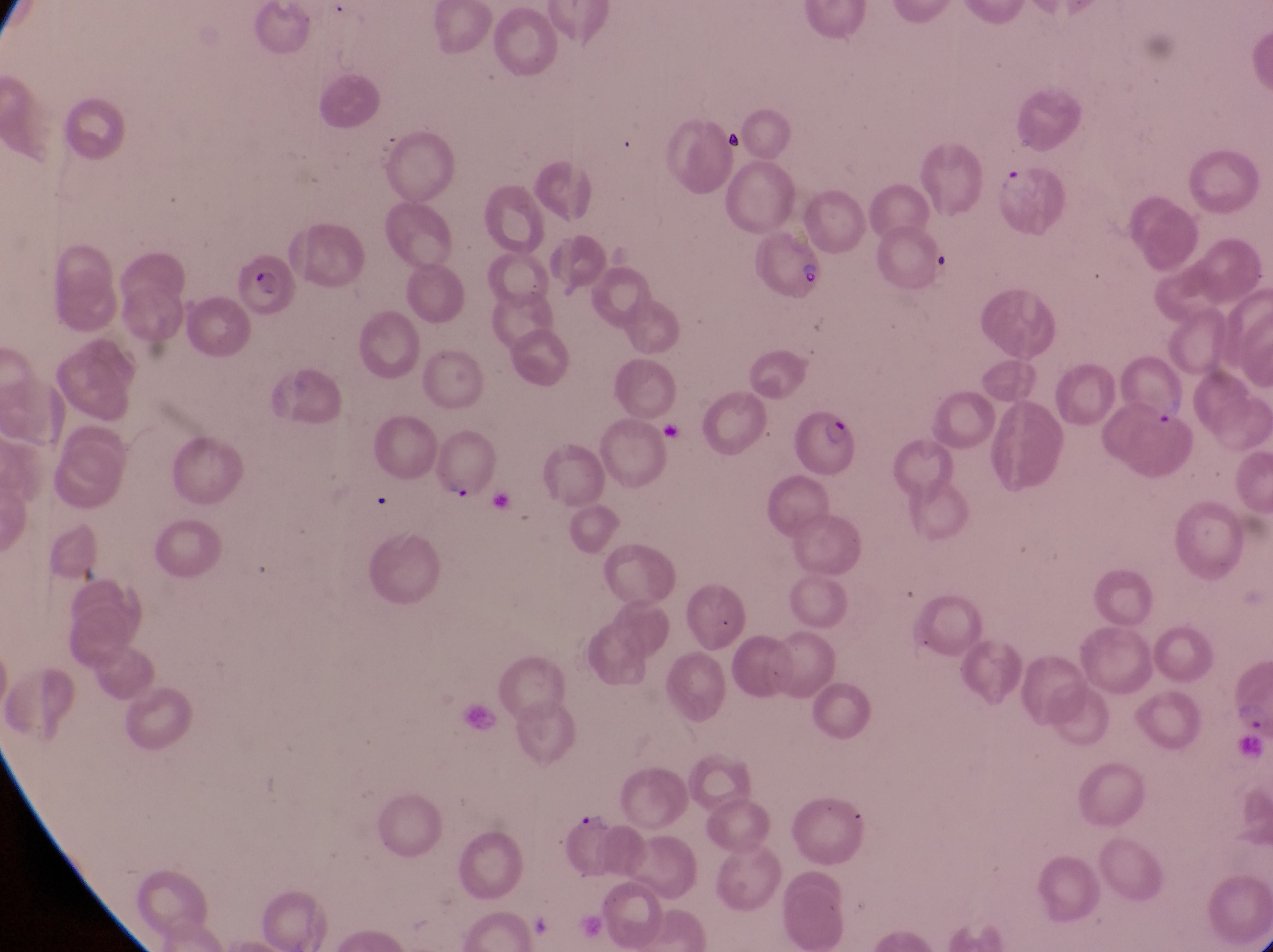

Approximate bounding boxes as (left, top, right, bottom) in pixels. Artifact (platelet-like body, stain precipitate, or debris) locations: (717, 123, 750, 155). Parasitised red blood cell locations: (996, 157, 1070, 240), (752, 223, 829, 298), (232, 262, 297, 324), (1120, 344, 1192, 429), (791, 404, 860, 479). Trophozoite locations: (444, 474, 477, 507), (1231, 696, 1270, 739), (576, 807, 613, 834). Image is 1273×952 pixels. Photographed through the eyepiece of an Olympus CX-23 microscope with a smartphone camera. Magnification of 1000x. Sample from Uganda. Thin blood smear. One field of view.